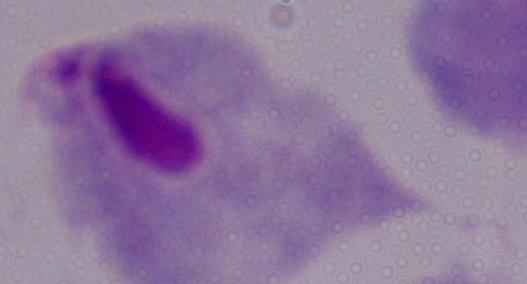 Micrograph. 1000x magnification. A trichomonad is seen.